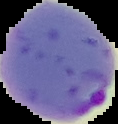

Summary:
  - Image size: 118×124 pixels
  - Result: Plasmodium parasites identified
  - Preparation: thin blood film
  - Image type: segmented cell region on a black background